Comment on the morphology of the red blood cells.
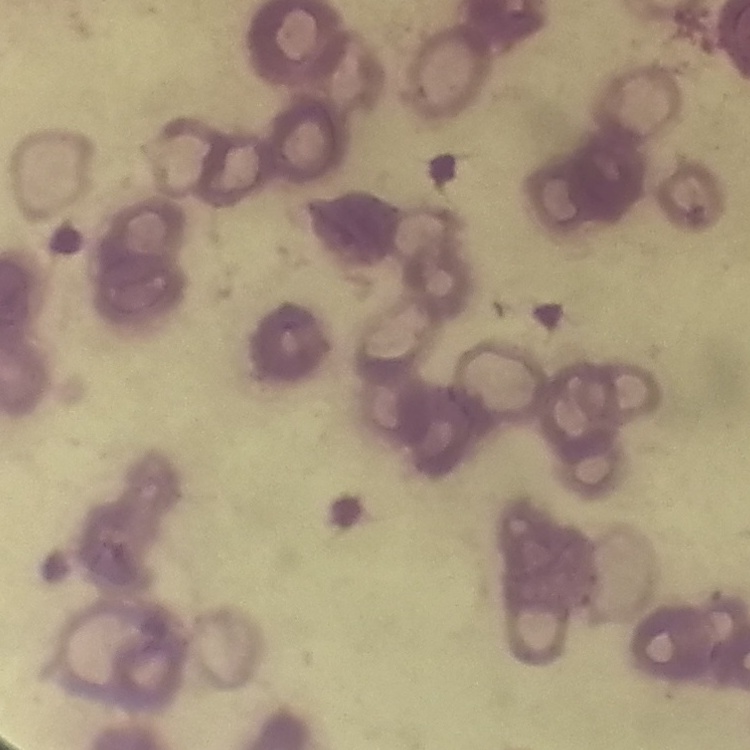
They show rouleaux formation.

stain: Field's or Giemsa
preparation: thin peripheral smear
image_type: one tile cut from a larger photomicrograph